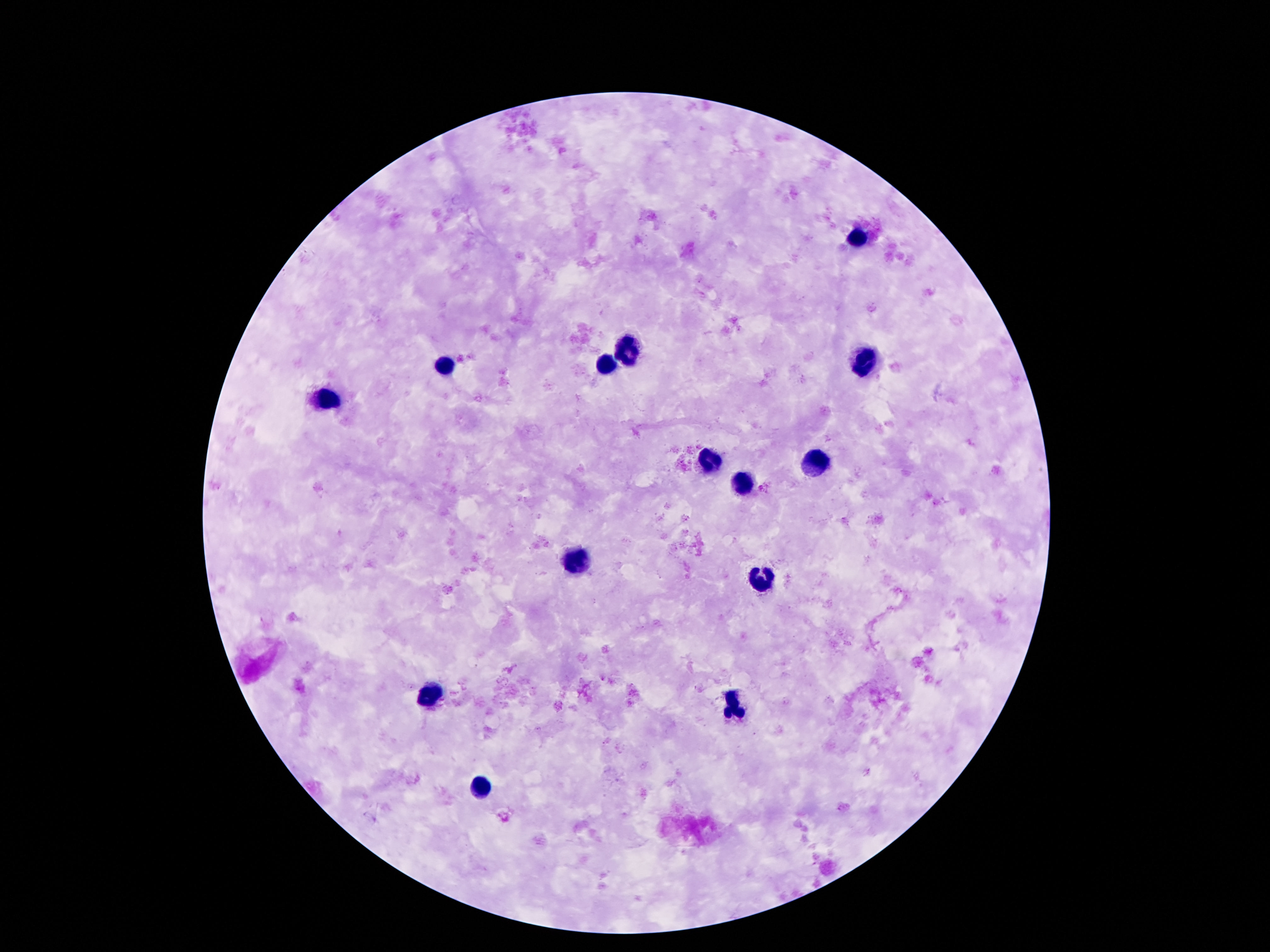

Approximate centers as {x, y} in pixels.
Summary:
  - Leukocyte locations: {859, 234}, {628, 345}, {864, 361}, {446, 365}, {602, 366}, {329, 398}, {815, 461}, {710, 463}, {750, 487}, {574, 563}, {764, 578}, {430, 692}, {733, 708}, {476, 786}
  - Capture: smartphone camera through the microscope eyepiece
  - Magnification: 100x
  - Preparation: thick blood film
  - Image size: 1270×952 pixels
  - Stain: Giemsa
  - Field of view: single
  - Patient malaria status: negative